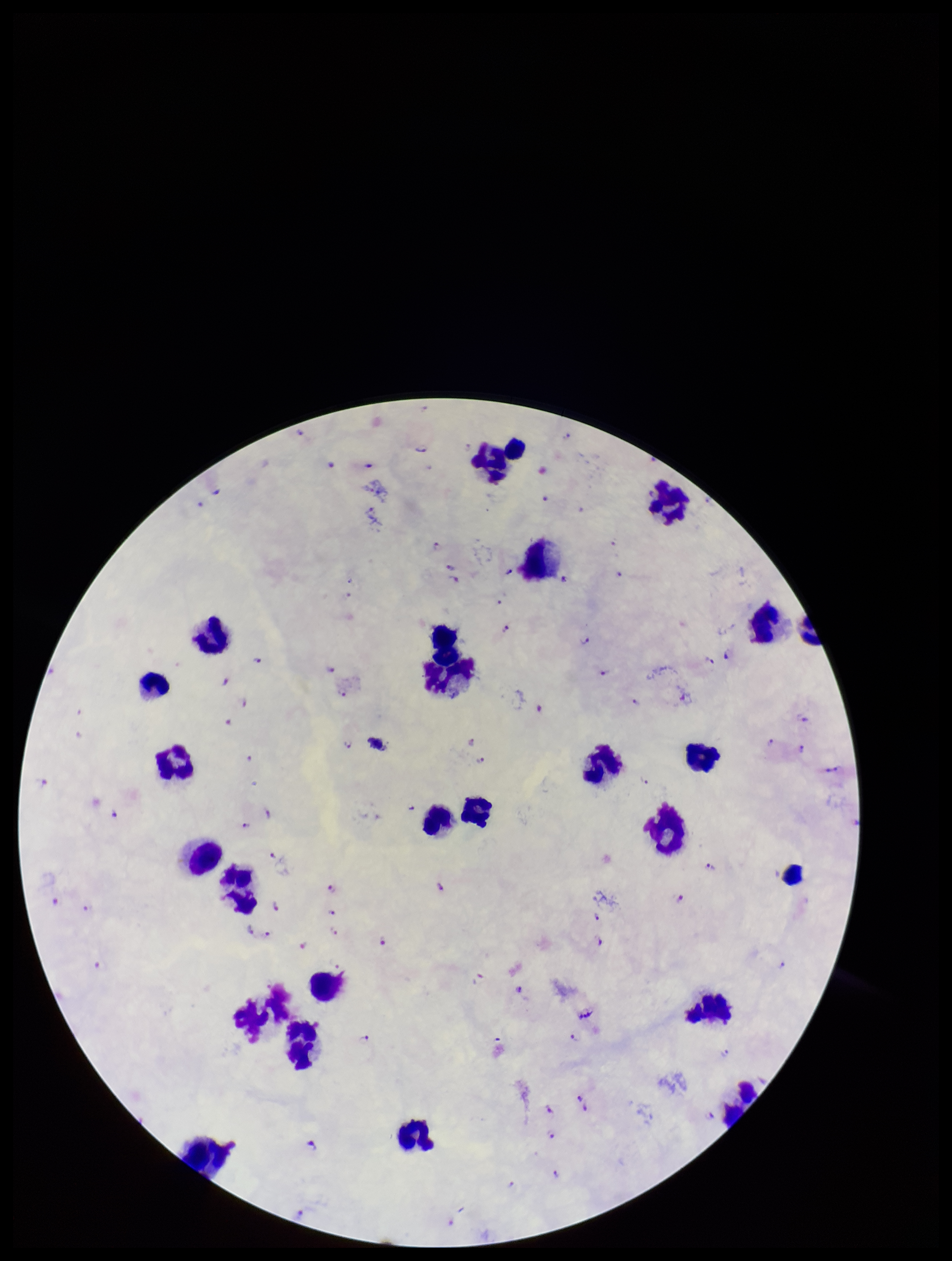

Summary:
  - Capture: smartphone photograph through the microscope eyepiece
  - Stain: Giemsa
  - Parasite count: 78
  - Field of view: single
  - Leukocyte count: 23
  - Patient malaria status: positive
  - Image size: 952×1261 pixels
  - Preparation: thick
  - Species reported for this patient: Plasmodium falciparum
  - Plasmodium parasites: identified